Name the parasite shown.
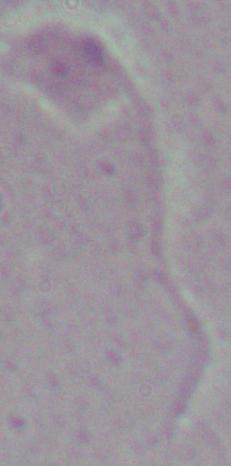
This is Leishmania.

magnification = 1000x
modality = photomicrograph